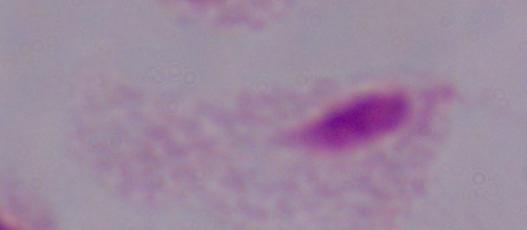

Summary:
  - Identification: trichomonad
  - Modality: micrograph
  - Magnification: 1000x